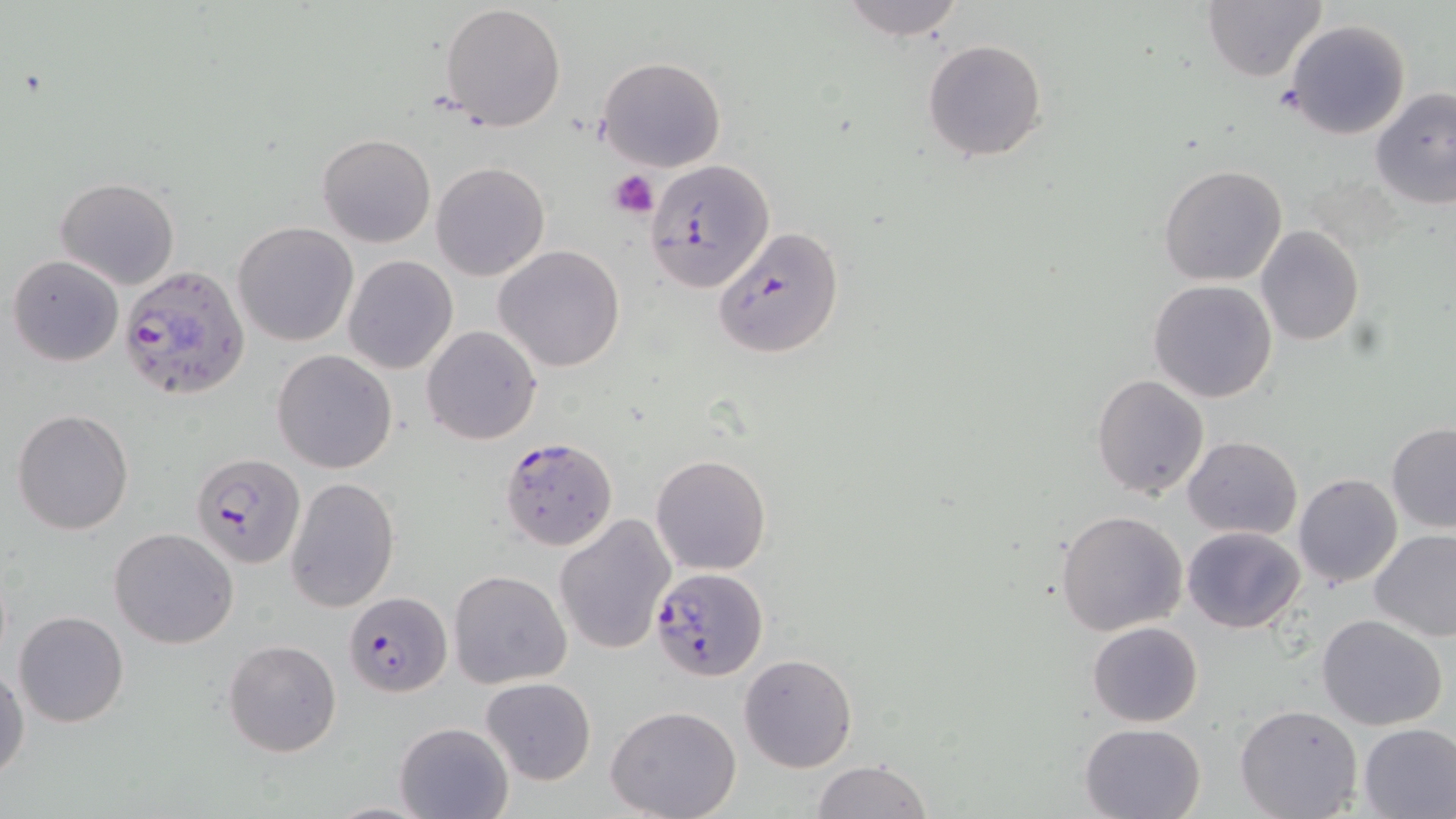
Approximate bounding boxes as (x1, y1, x2, y2) in pixels. Plasmodium falciparum-infected red blood cell locations: (648, 159, 778, 292), (118, 264, 250, 401), (498, 435, 618, 553), (190, 450, 304, 570), (650, 565, 767, 681), (343, 594, 451, 697). Uninfected red blood cell locations: (837, 0, 967, 40), (1199, 0, 1327, 83), (440, 4, 567, 132), (1283, 18, 1411, 141), (922, 38, 1047, 162), (597, 56, 727, 172), (1370, 88, 1456, 210), (316, 134, 435, 248), (430, 163, 550, 281), (1157, 164, 1287, 286), (55, 177, 180, 289), (232, 221, 358, 348), (1256, 225, 1364, 345), (712, 226, 846, 359), (494, 244, 625, 372), (8, 255, 123, 366), (342, 255, 459, 374), (1148, 279, 1279, 403), (421, 325, 542, 445), (272, 349, 398, 474), (1091, 372, 1210, 498), (12, 408, 134, 536), (1386, 422, 1456, 531), (1184, 434, 1302, 539), (650, 454, 772, 575), (1293, 474, 1401, 589), (285, 476, 399, 613), (1056, 509, 1189, 636), (553, 512, 675, 655), (1182, 526, 1306, 632), (109, 527, 238, 648), (1369, 528, 1456, 641), (449, 570, 572, 689), (12, 610, 129, 727), (1316, 614, 1448, 731), (1087, 621, 1203, 727), (224, 638, 342, 757), (737, 653, 857, 773), (1, 663, 27, 780), (481, 677, 596, 785), (1234, 703, 1364, 818), (605, 706, 742, 819), (393, 721, 514, 819), (1079, 722, 1206, 819), (1358, 722, 1456, 818), (811, 760, 932, 819). Platelet locations: (609, 169, 660, 220). Slide-level diagnosis: Plasmodium falciparum. May-Grünwald-Giemsa-stained preparation. Thin blood smear. Single field of view. Light microscopy. 1000x magnification. Image is 1456×819 pixels.